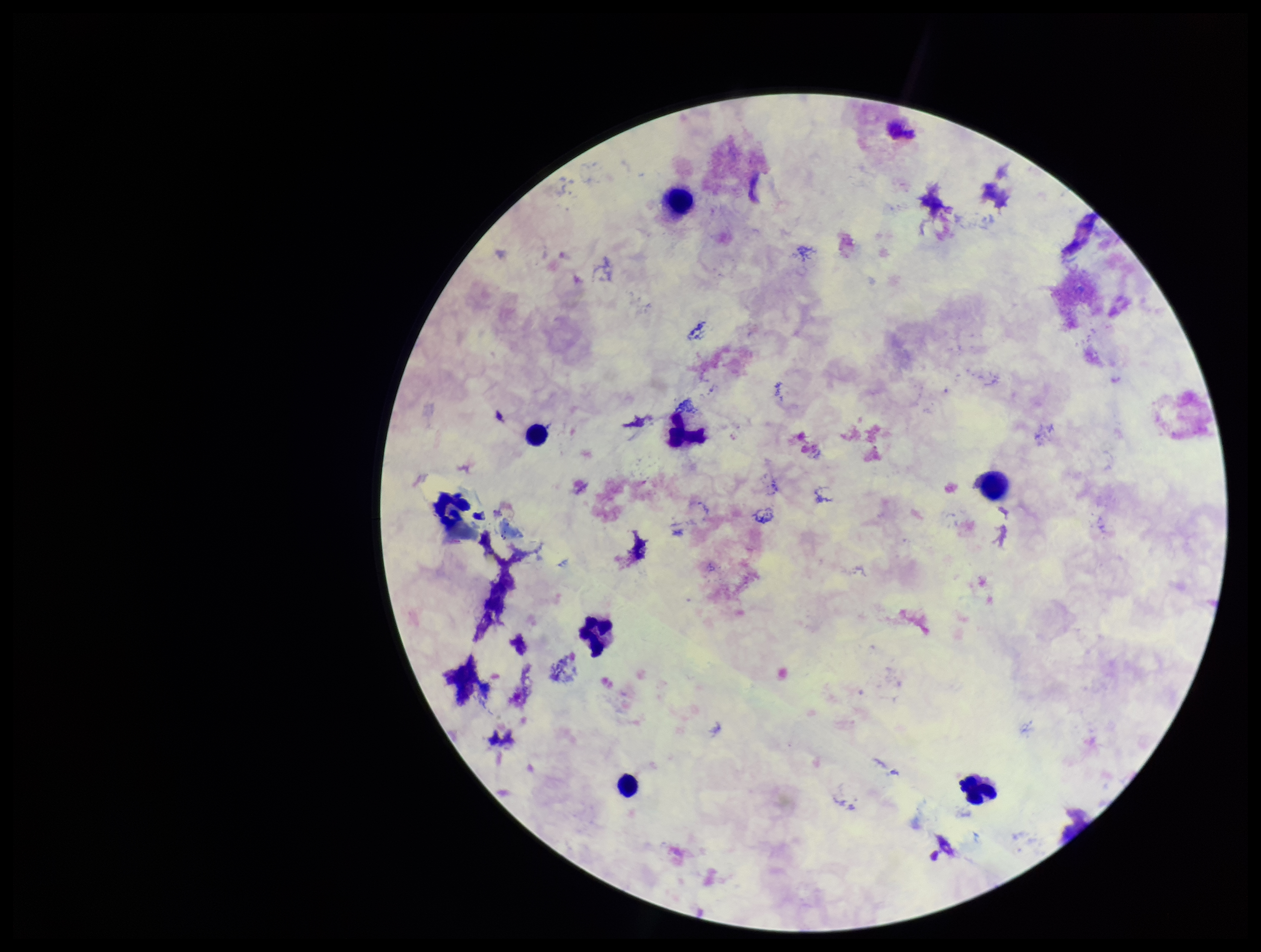 Patient malaria status: negative. Stained with Giemsa. Parasite count: 0. One field from this slide. Plasmodium parasites: none identified. Photographed through the microscope eyepiece with a smartphone camera. Preparation: thick. Image is 1261×952 pixels. Leukocyte count: 7.